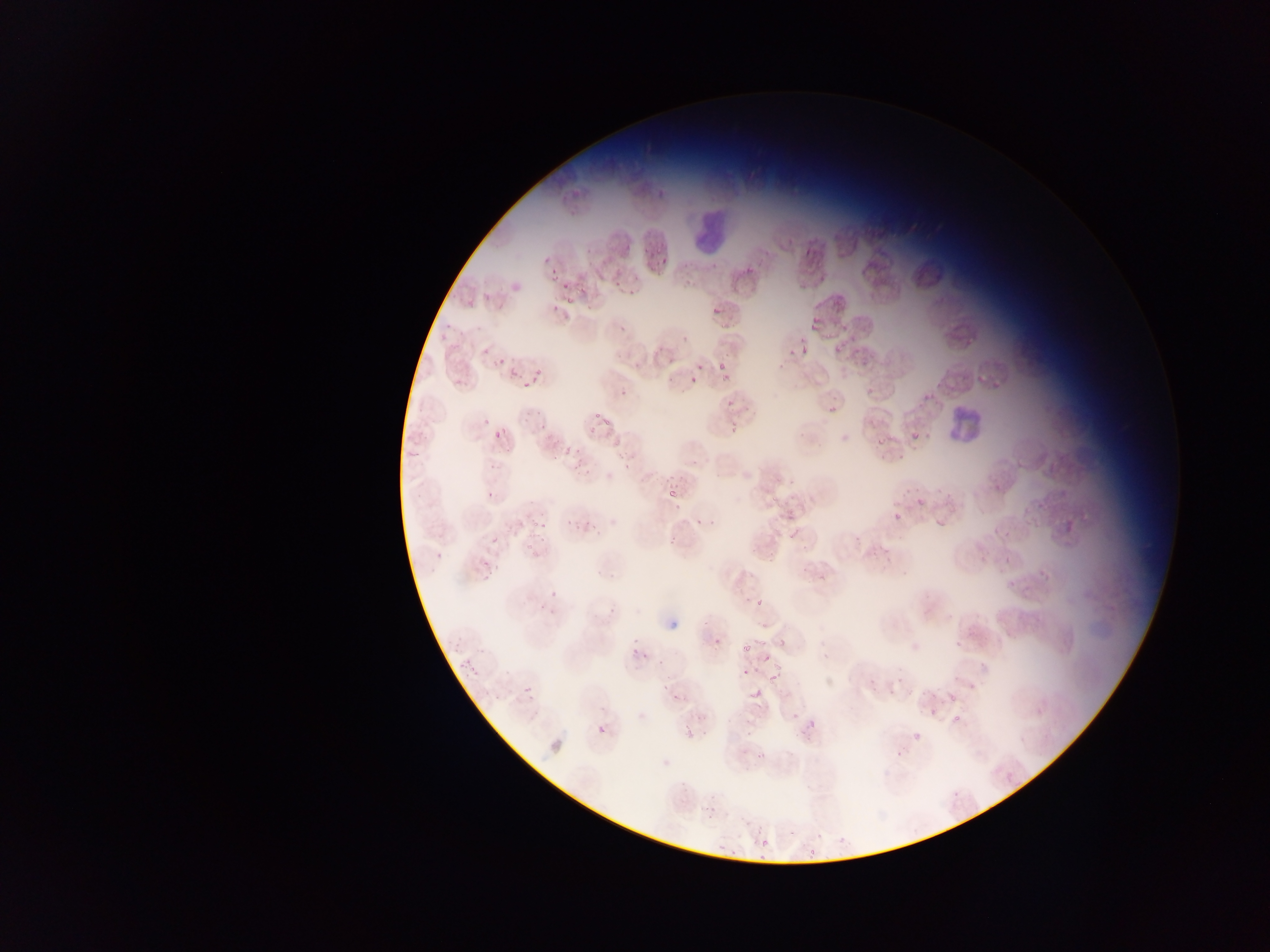
Approximate bounding boxes as {left, top, right, bottom} in pixels. Malaria parasite locations: {653, 243, 666, 255}, {543, 247, 556, 265}, {652, 255, 673, 269}, {710, 259, 718, 270}, {739, 267, 756, 279}, {681, 271, 693, 283}, {550, 274, 560, 280}, {612, 277, 626, 287}, {626, 279, 639, 298}, {558, 281, 574, 291}, {582, 282, 591, 299}, {480, 289, 493, 306}, {562, 293, 577, 306}, {492, 302, 506, 313}, {710, 303, 721, 314}, {551, 304, 561, 314}, {809, 314, 827, 332}, {443, 322, 452, 330}, {615, 323, 629, 334}, {824, 329, 836, 339}, {680, 333, 690, 341}, {438, 335, 446, 342}, {834, 340, 844, 355}, {482, 343, 493, 356}, {654, 343, 669, 354}, {798, 344, 809, 360}, {786, 347, 795, 356}, {493, 353, 509, 364}, {669, 354, 677, 360}, {717, 354, 731, 369}, {778, 359, 792, 374}, {694, 365, 702, 373}, {509, 367, 520, 378}, {528, 367, 543, 378}, {721, 370, 732, 382}, {687, 376, 700, 386}, {525, 377, 543, 385}, {619, 379, 632, 396}, {520, 382, 526, 392}, {723, 393, 736, 411}, {828, 405, 835, 414}, {594, 408, 607, 420}, {534, 409, 542, 418}, {601, 417, 613, 429}, {537, 421, 550, 432}, {728, 423, 737, 436}, {585, 425, 598, 432}, {489, 426, 504, 440}, {911, 432, 921, 440}, {609, 434, 628, 451}, {880, 434, 888, 444}, {407, 446, 427, 457}, {561, 446, 573, 456}, {880, 451, 891, 460}, {552, 452, 564, 460}, {572, 454, 591, 474}, {897, 454, 907, 460}, {620, 457, 644, 474}, {488, 461, 500, 472}, {664, 470, 676, 487}, {787, 470, 803, 487}, {903, 485, 919, 494}, {485, 488, 497, 499}, {666, 491, 679, 508}, {768, 492, 775, 505}, {914, 498, 929, 507}, {784, 504, 796, 520}, {1023, 507, 1038, 526}, {565, 511, 580, 527}, {893, 512, 905, 521}, {584, 513, 602, 537}, {697, 513, 704, 524}, {531, 518, 537, 529}, {935, 518, 945, 528}, {541, 519, 548, 533}, {708, 521, 715, 529}, {785, 526, 798, 539}, {540, 531, 547, 545}, {1001, 532, 1007, 540}, {850, 533, 862, 542}, {667, 535, 675, 546}, {490, 536, 501, 548}, {524, 538, 538, 553}, {764, 543, 782, 565}, {751, 545, 760, 555}, {884, 551, 896, 562}, {435, 552, 444, 561}, {1003, 554, 1012, 571}, {482, 561, 492, 567}, {799, 565, 810, 576}, {1034, 569, 1047, 577}, {816, 570, 833, 586}, {480, 571, 493, 582}, {1007, 574, 1021, 587}, {552, 589, 567, 600}, {754, 590, 766, 609}, {606, 600, 620, 615}, {538, 605, 558, 615}, {701, 618, 715, 630}, {950, 632, 965, 653}, {709, 634, 727, 646}, {453, 635, 464, 653}, {753, 635, 769, 645}, {776, 638, 787, 651}, {737, 641, 757, 655}, {475, 646, 487, 653}, {631, 646, 647, 660}, {763, 654, 771, 661}, {463, 660, 479, 678}, {773, 660, 783, 672}, {740, 668, 752, 680}, {658, 674, 682, 694}, {868, 675, 880, 687}, {896, 676, 904, 685}, {767, 678, 777, 686}, {522, 684, 534, 695}, {888, 685, 898, 696}, {749, 687, 762, 699}, {671, 692, 685, 706}, {489, 693, 506, 705}, {948, 693, 960, 704}, {926, 707, 940, 716}, {1035, 707, 1044, 717}, {803, 711, 815, 731}, {791, 712, 801, 721}, {953, 712, 965, 722}, {594, 716, 610, 735}, {745, 724, 756, 737}, {911, 728, 927, 739}, {755, 748, 772, 766}, {894, 751, 906, 759}, {1005, 773, 1014, 782}, {952, 790, 963, 800}, {701, 800, 721, 822}, {754, 823, 766, 835}, {786, 827, 795, 840}, {812, 830, 828, 839}, {835, 832, 849, 844}, {713, 838, 729, 854}, {760, 838, 770, 848}, {727, 846, 743, 862}, {807, 846, 818, 863}, {753, 853, 767, 861} | approximate {x, y} pixel centers of objects too small to bound: {486, 423}, {882, 552}, {432, 570}. Leukocyte locations: {678, 193, 739, 246}, {931, 387, 992, 448}. Photographed through a microscope with a mobile-phone camera. Thin blood smear. Sample from Ghana. One field of view. Image is 1270×952 pixels.